Outline each blood parasite and name the species.
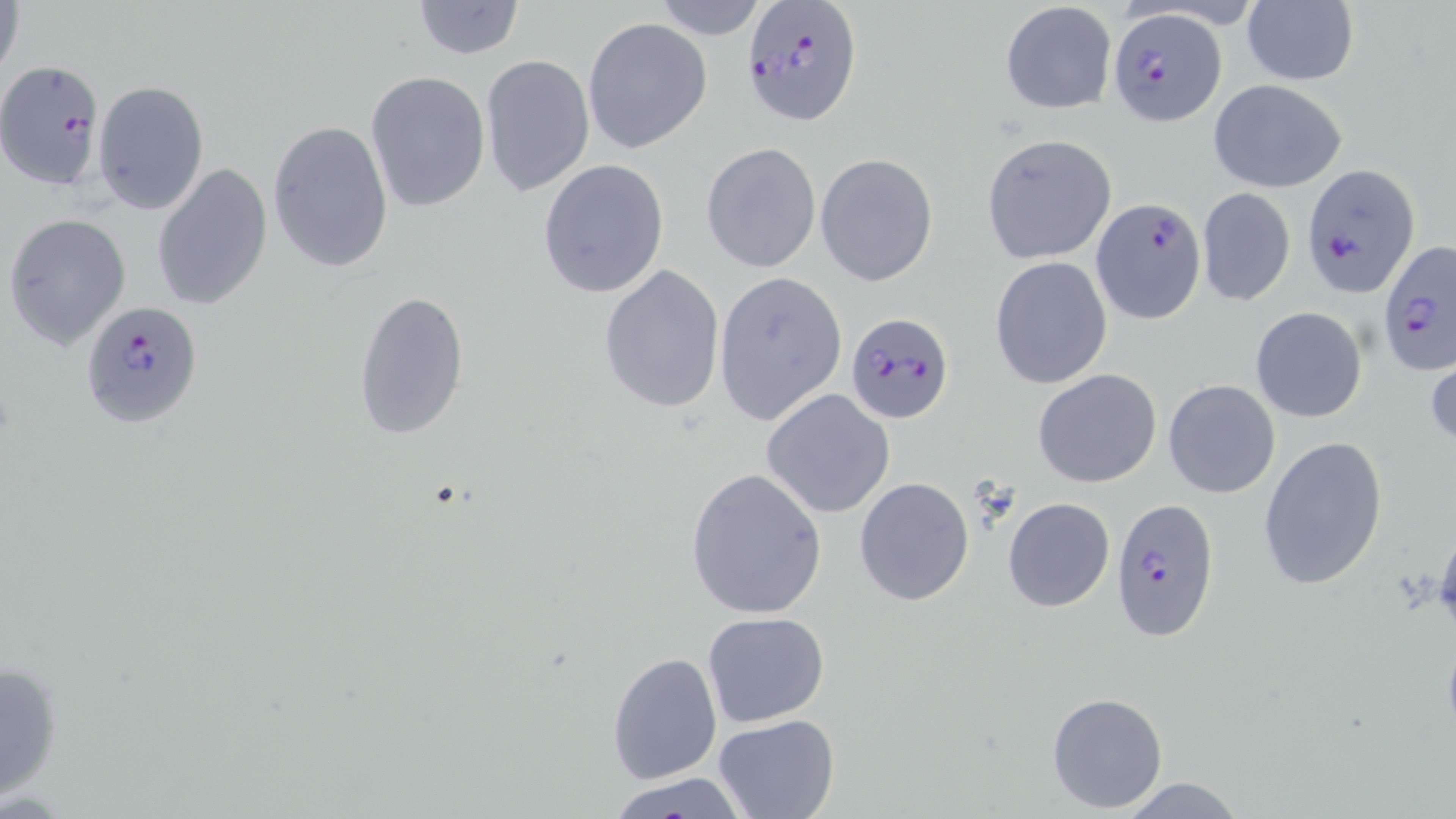
Approximate bounding boxes as (x1,y1)-(x2,y2) corner pairs in pixels.
Plasmodium falciparum-infected red blood cells: (740,0)-(862,126), (1107,8)-(1225,127), (0,59)-(106,191), (1303,164)-(1422,295), (1091,197)-(1207,323), (1378,240)-(1454,373), (79,299)-(203,430), (845,311)-(954,425), (1109,497)-(1222,642).
No Plasmodium ovale, Plasmodium malariae, Plasmodium vivax, Babesia divergens, or Trypanosoma brucei observed.

Summary:
  - Uninfected red blood cell locations: (649,0)-(768,40), (1,1)-(25,86), (412,1)-(526,59), (999,1)-(1117,115), (1241,2)-(1359,86), (583,17)-(712,154), (480,54)-(594,197), (365,71)-(491,214), (1208,79)-(1347,193), (92,80)-(209,215), (267,119)-(395,277), (980,134)-(1116,263), (701,142)-(821,273), (815,153)-(939,288), (538,158)-(669,299), (151,163)-(273,310), (1196,187)-(1296,307), (3,213)-(131,350), (990,255)-(1113,390), (599,265)-(726,414), (713,271)-(846,425), (355,288)-(470,440), (1250,307)-(1368,424), (1426,349)-(1456,453), (1033,368)-(1162,488), (1162,380)-(1281,499), (761,389)-(896,519), (1258,435)-(1387,590), (685,466)-(828,620), (855,476)-(975,607), (1002,497)-(1115,611), (1430,532)-(1456,631), (702,610)-(832,729), (606,650)-(722,782), (1,657)-(65,801), (1046,691)-(1168,813), (714,712)-(840,818), (604,775)-(754,818), (1116,776)-(1247,818)
  - Slide-level diagnosis: Plasmodium falciparum
  - Image size: 1456×819 pixels
  - Modality: optical microscopy
  - Preparation: thin blood film
  - Stain: May-Grünwald-Giemsa
  - Magnification: 1000x
  - Field of view: one of a larger specimen